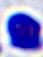
A white blood cell is seen. Micrograph. Captured at 400x magnification.